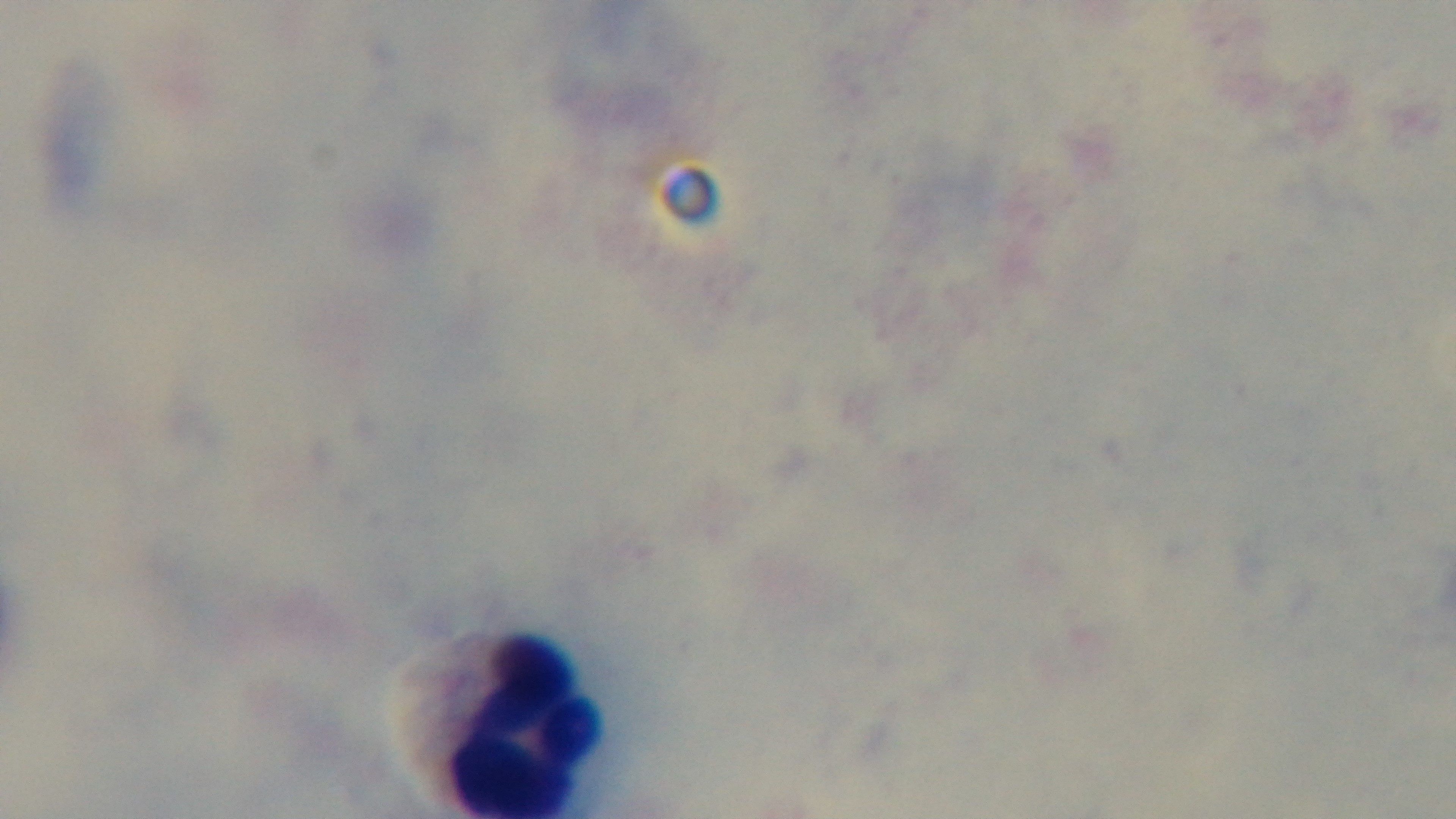

Summary:
  - Capture: mounted 4K digital camera
  - Objective: 100x oil immersion
  - Malaria status: uninfected
  - Modality: light microscopy
  - Field of view: one from the slide
  - Stain: Giemsa
  - Preparation: thick blood film